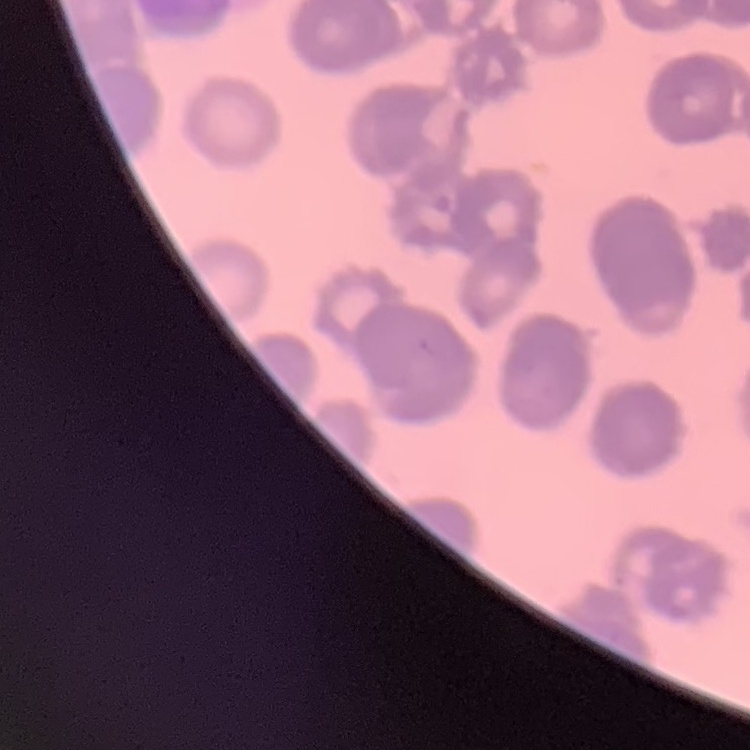

Summary:
  - Erythrocyte morphology: rouleaux formation
  - Stain: Field's or Giemsa
  - Preparation: thin peripheral smear
  - Image type: one tile cut from a larger photomicrograph